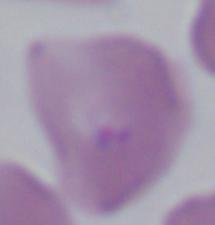 Micrograph. A Babesia parasite is seen. 1000x magnification.